Identify the parasite.
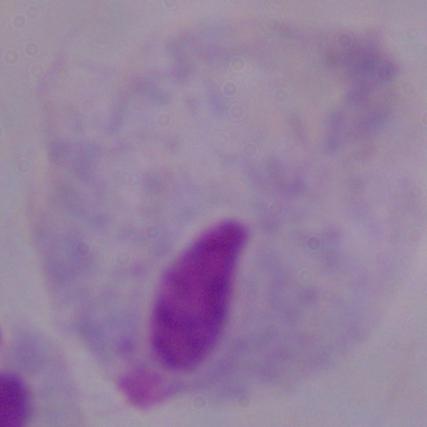
This is a trichomonad.

Summary:
  - Modality: micrograph
  - Magnification: 1000x